Outline each Trypanosoma brucei.
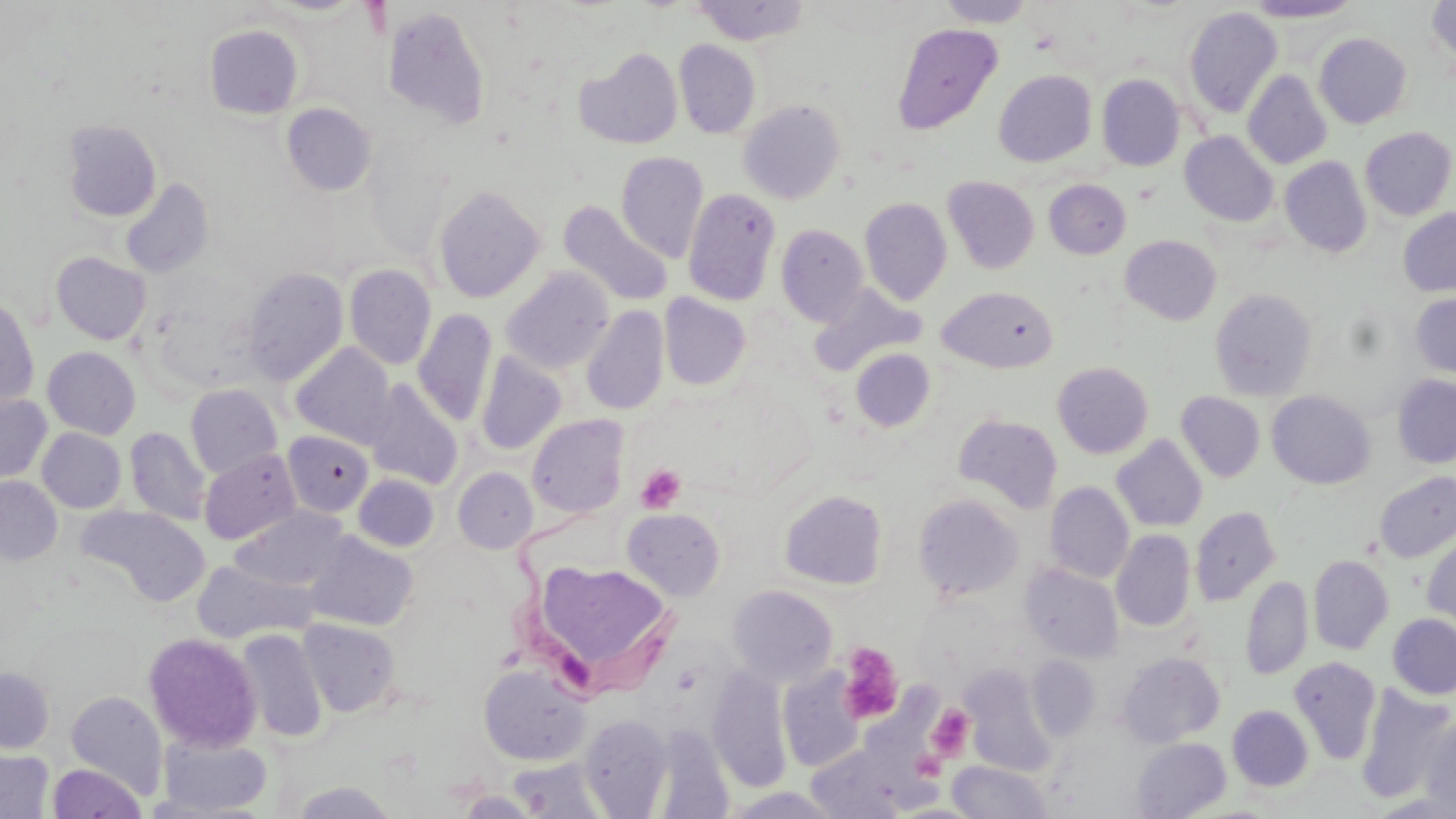
Approximate bounding boxes as (x1, y1, x2, y2) in pixels.
Trypanosoma brucei: (500, 511, 688, 703).

slide_level_diagnosis: Trypanosoma brucei
modality: optical microscopy
preparation: thin blood film
platelet_locations: 'approximate bounding boxes as (x1, y1, x2, y2) in pixels: (636, 464, 685, 513), (838, 642, 904, 724), (928, 706, 973, 760)'
magnification: 1000x
field_of_view: one of a larger specimen
image_size: 1456×819 pixels
uninfected_red_blood_cell_locations: 'approximate bounding boxes as (x1, y1, x2, y2) in pixels: (692, 0, 810, 45), (935, 0, 1037, 27), (1242, 0, 1361, 22), (1428, 0, 1456, 67), (382, 5, 492, 133), (1184, 6, 1283, 119), (891, 22, 1004, 135), (204, 24, 304, 119), (1314, 32, 1412, 129), (674, 40, 760, 139), (575, 47, 683, 149), (994, 70, 1096, 167), (1243, 70, 1332, 169), (1097, 75, 1185, 170), (738, 99, 845, 204), (282, 103, 376, 196), (61, 119, 162, 222), (1360, 127, 1455, 220), (1180, 131, 1278, 226), (616, 152, 708, 263), (1280, 156, 1372, 257), (943, 176, 1040, 274), (120, 177, 214, 279), (1044, 179, 1131, 258), (433, 184, 545, 303), (682, 188, 781, 306), (859, 197, 952, 305), (559, 201, 673, 307), (1398, 208, 1456, 297), (776, 223, 868, 327), (1120, 235, 1221, 325), (51, 251, 151, 345), (344, 264, 436, 370), (243, 267, 348, 385), (501, 267, 614, 374), (810, 284, 925, 375), (937, 286, 1058, 373), (1210, 289, 1317, 401), (1410, 293, 1456, 378), (659, 294, 750, 390), (0, 295, 39, 409), (581, 305, 669, 416), (413, 309, 497, 427), (291, 343, 397, 448), (42, 346, 140, 439), (850, 349, 935, 432), (475, 351, 567, 455), (1053, 362, 1153, 459), (1392, 374, 1456, 469), (365, 380, 464, 490), (185, 384, 283, 479), (1267, 391, 1376, 489), (0, 392, 52, 482), (1176, 392, 1265, 483), (527, 414, 629, 519), (953, 414, 1063, 514), (125, 426, 210, 525), (37, 428, 126, 513), (283, 430, 374, 517), (1112, 435, 1207, 532), (199, 449, 301, 544), (453, 467, 538, 554), (1375, 471, 1456, 563), (353, 474, 440, 551), (0, 476, 63, 566), (1044, 482, 1134, 583), (779, 490, 888, 590), (914, 494, 1023, 602), (76, 505, 209, 606), (231, 505, 349, 591), (1190, 507, 1281, 606), (623, 508, 725, 600), (1422, 529, 1456, 633), (1111, 530, 1195, 632), (304, 531, 418, 630), (1309, 554, 1394, 655), (193, 559, 317, 643), (538, 560, 675, 661), (1020, 563, 1123, 663), (1241, 575, 1313, 680), (728, 585, 837, 687), (1387, 613, 1456, 699), (297, 618, 402, 716), (236, 629, 328, 741), (144, 632, 263, 752), (1118, 652, 1224, 747), (1028, 656, 1100, 742), (1288, 656, 1382, 765), (478, 663, 590, 766), (961, 665, 1057, 777), (707, 666, 791, 792), (0, 667, 54, 752), (779, 669, 864, 772), (1355, 684, 1456, 805), (65, 690, 167, 797), (1228, 705, 1313, 791), (579, 713, 673, 817), (1420, 717, 1456, 818), (157, 734, 271, 816), (1131, 737, 1231, 818), (805, 744, 924, 819), (0, 749, 54, 818), (946, 761, 1054, 818), (48, 763, 146, 819), (289, 781, 398, 818), (723, 787, 846, 818), (456, 791, 541, 817)'
stain: May-Grünwald-Giemsa